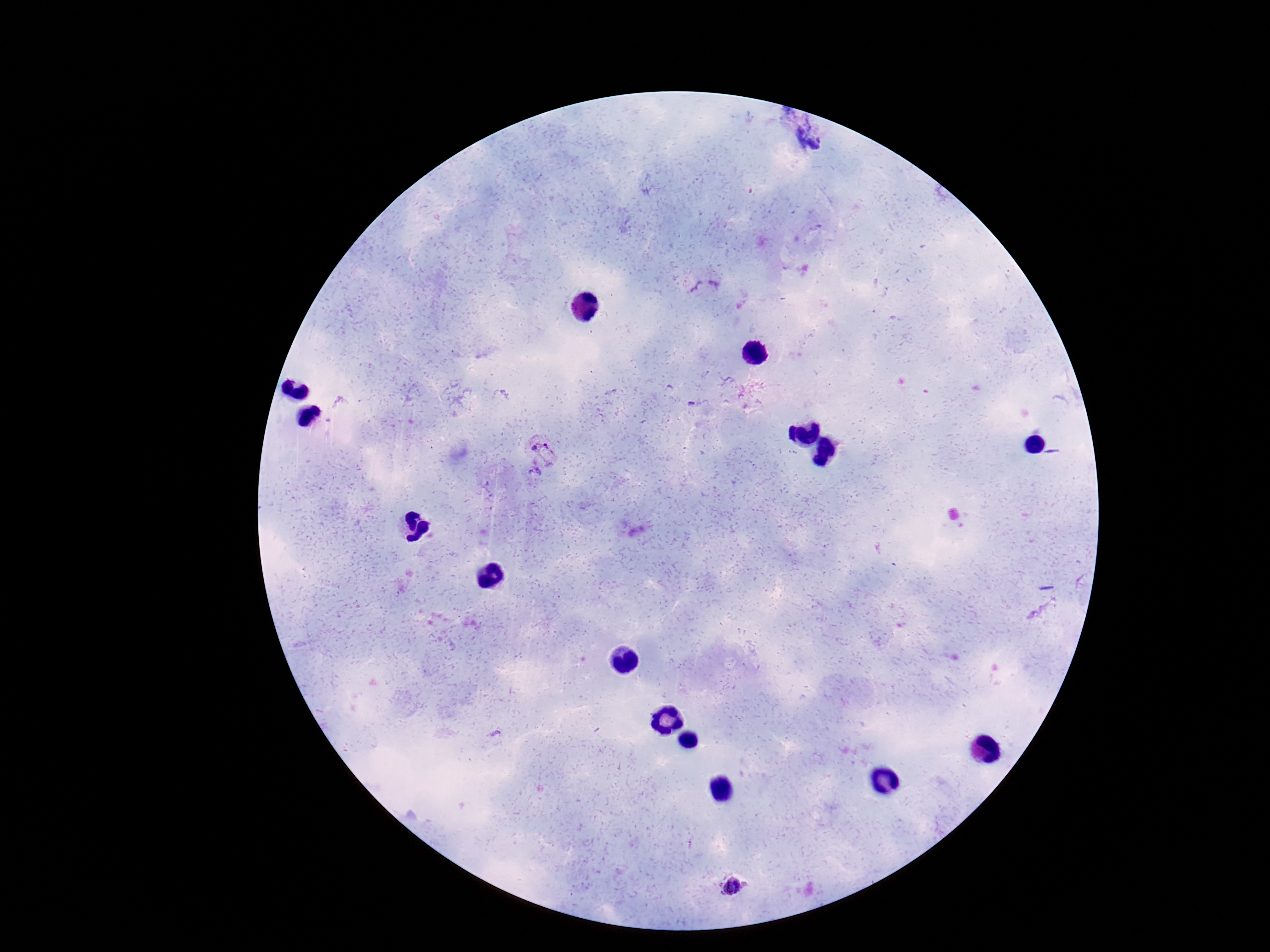
Approximate object centers, in pixels from the top-left corner. Plasmodium parasite locations: (x=704, y=284), (x=543, y=451), (x=733, y=887). 100x magnification. Thick peripheral-blood smear. Patient malaria status: infected. Giemsa stain. Photographed through the microscope eyepiece with a smartphone camera. Image is 1270×952 pixels. One field from this slide.